Classify this cell by malaria status.
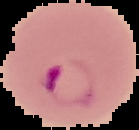
It is parasitized.

Summary:
  - Image size: 139×130 pixels
  - Image type: cell region segmented out of the field of view; surrounding area masked to black
  - Preparation: thin blood film